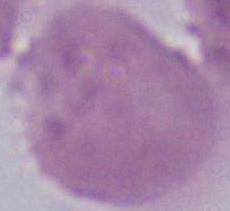

Summary:
  - Magnification: 1000x
  - Identification: erythrocyte
  - Modality: photomicrograph